Classify this cell by malaria status.
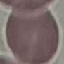

It is uninfected.

Summary:
  - Preparation: thin blood smear
  - Capture: smartphone camera at the microscope eyepiece
  - Stain: Giemsa
  - Image type: automatically extracted cell patch, resized to 64 × 64 pixels